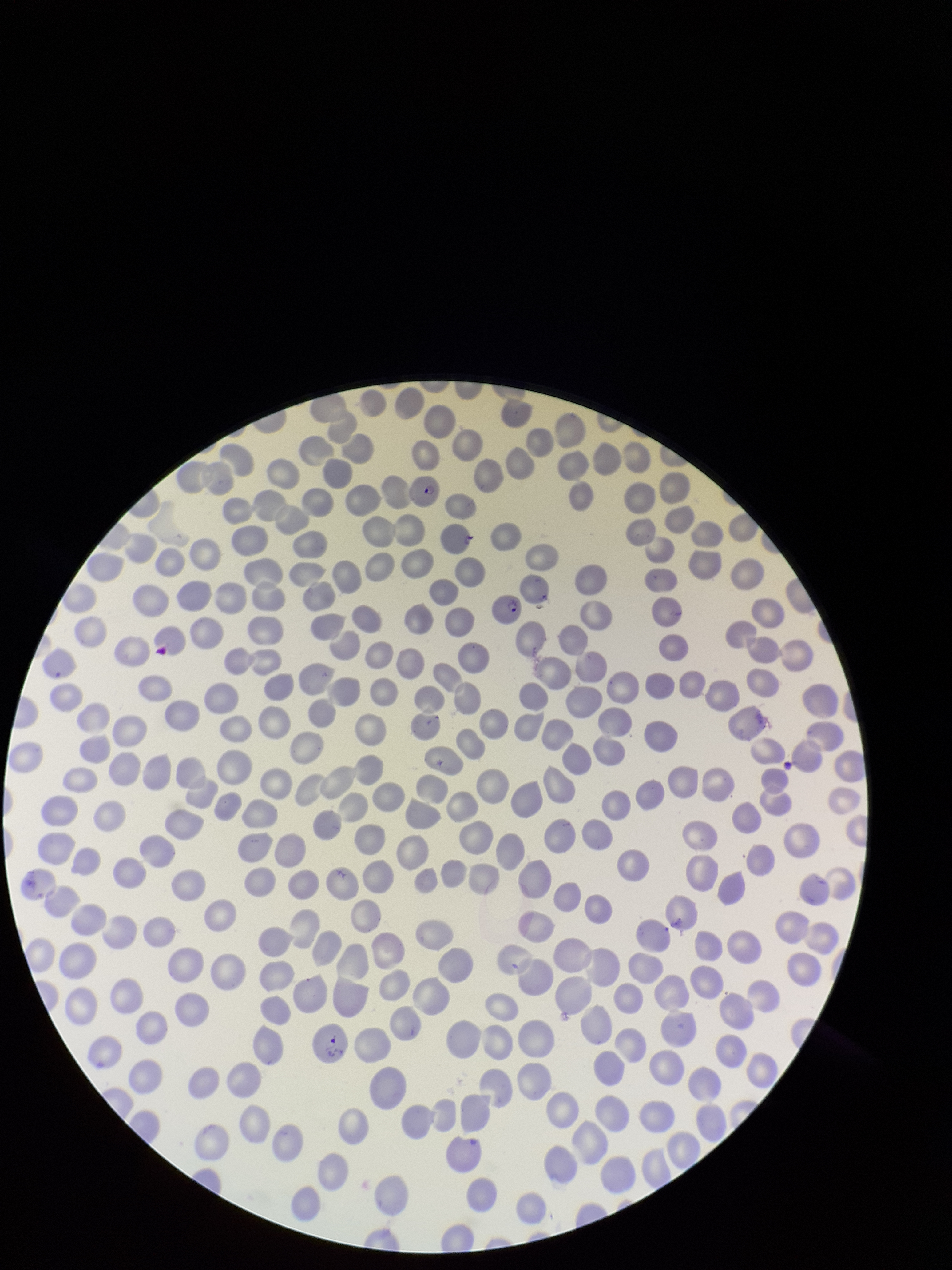

{
  "parasitized_red_blood_cell_count": 3,
  "species_reported_for_this_patient": "Plasmodium falciparum",
  "preparation": "thin blood smear",
  "red_blood_cell_count": 283,
  "parasitized_red_blood_cells": "detected",
  "patient_malaria_status": "infected",
  "image_size": "952×1270 pixels",
  "stain": "Giemsa",
  "field_of_view": "single",
  "capture": "smartphone photograph through the microscope eyepiece"
}